Report the malaria status of this cell.
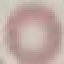
It is uninfected.

Acquired by smartphone through the microscope eyepiece. Thin blood film. Giemsa-stained preparation. Cell patch, automatically extracted from a larger field of view and resized to 64 × 64 pixels.